Identify the preparation type.
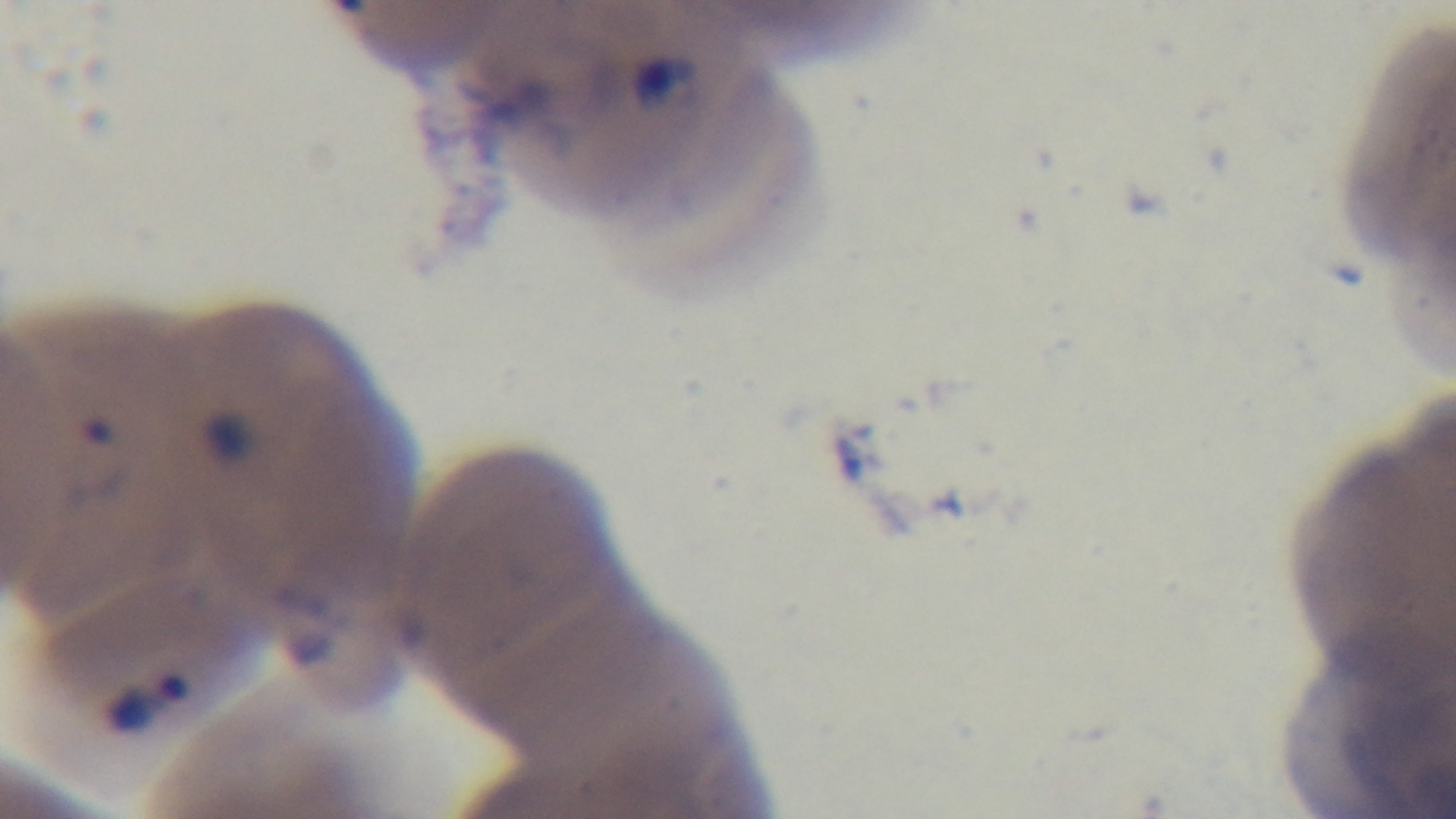

Thin.

Photomicrograph. One field from the slide. Malaria status: positive. Oil-immersion objective, 100x. Captured with a mounted 4K digital camera. Giemsa-stained.